Identify the blood parasite species.
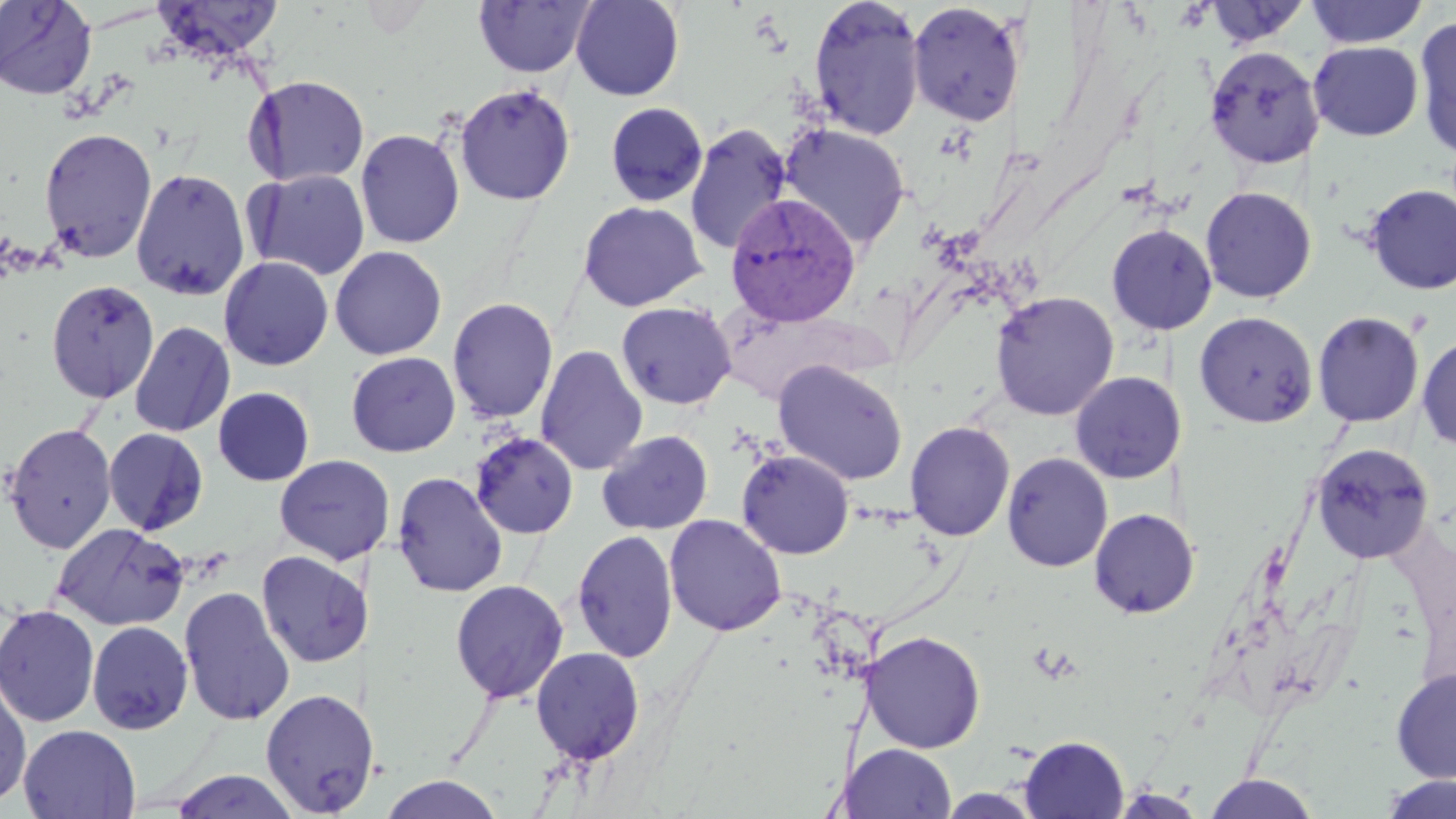

Plasmodium vivax.

Approximate bounding boxes as (x1,y1)-(x2,y2) corner pairs in pixels. Plasmodium vivax-infected red blood cell locations: (724,193)-(860,326). Uninfected red blood cell locations: (0,0)-(97,100), (570,0)-(684,101), (808,0)-(926,140), (1305,0)-(1428,48), (151,1)-(285,61), (473,1)-(595,79), (1202,1)-(1314,49), (907,2)-(1024,126), (1414,16)-(1456,159), (1309,41)-(1423,141), (1204,45)-(1324,169), (244,74)-(371,188), (454,83)-(576,206), (605,101)-(708,207), (685,122)-(792,255), (777,123)-(911,250), (38,127)-(157,263), (355,128)-(465,249), (131,167)-(251,301), (246,168)-(371,281), (1362,184)-(1456,295), (1200,186)-(1317,304), (577,200)-(707,311), (1105,223)-(1218,336), (329,245)-(447,361), (218,256)-(334,371), (46,279)-(159,402), (989,291)-(1119,420), (447,296)-(559,423), (616,301)-(736,409), (1194,311)-(1318,428), (1312,311)-(1425,428), (129,321)-(235,438), (1416,333)-(1456,452), (535,344)-(648,476), (346,351)-(461,458), (772,359)-(909,485), (1071,371)-(1179,484), (213,387)-(315,486), (904,420)-(1015,541), (2,422)-(117,553), (103,427)-(209,536), (596,429)-(714,535), (470,432)-(579,539), (1311,442)-(1435,564), (736,449)-(855,559), (1002,452)-(1113,572), (273,455)-(389,565), (392,471)-(508,597), (1089,508)-(1199,619), (664,514)-(787,636), (51,522)-(190,631), (571,529)-(678,663), (257,550)-(366,668), (449,579)-(568,704), (178,586)-(296,727), (0,604)-(100,727), (87,621)-(194,735), (860,630)-(986,753), (530,646)-(645,766), (1391,667)-(1456,783), (0,671)-(32,809), (259,688)-(370,817), (18,724)-(141,819), (1019,735)-(1129,818), (845,743)-(955,818), (168,769)-(303,818), (1201,773)-(1321,818), (381,774)-(506,818), (1379,774)-(1456,819), (1106,785)-(1211,817), (937,788)-(1044,818). One field of a larger specimen. Image is 1456×819 pixels. May-Grünwald-Giemsa-stained preparation. Light microscopy. Thin blood film. 1000x magnification.